Give the extent of all uninfected red blood cells.
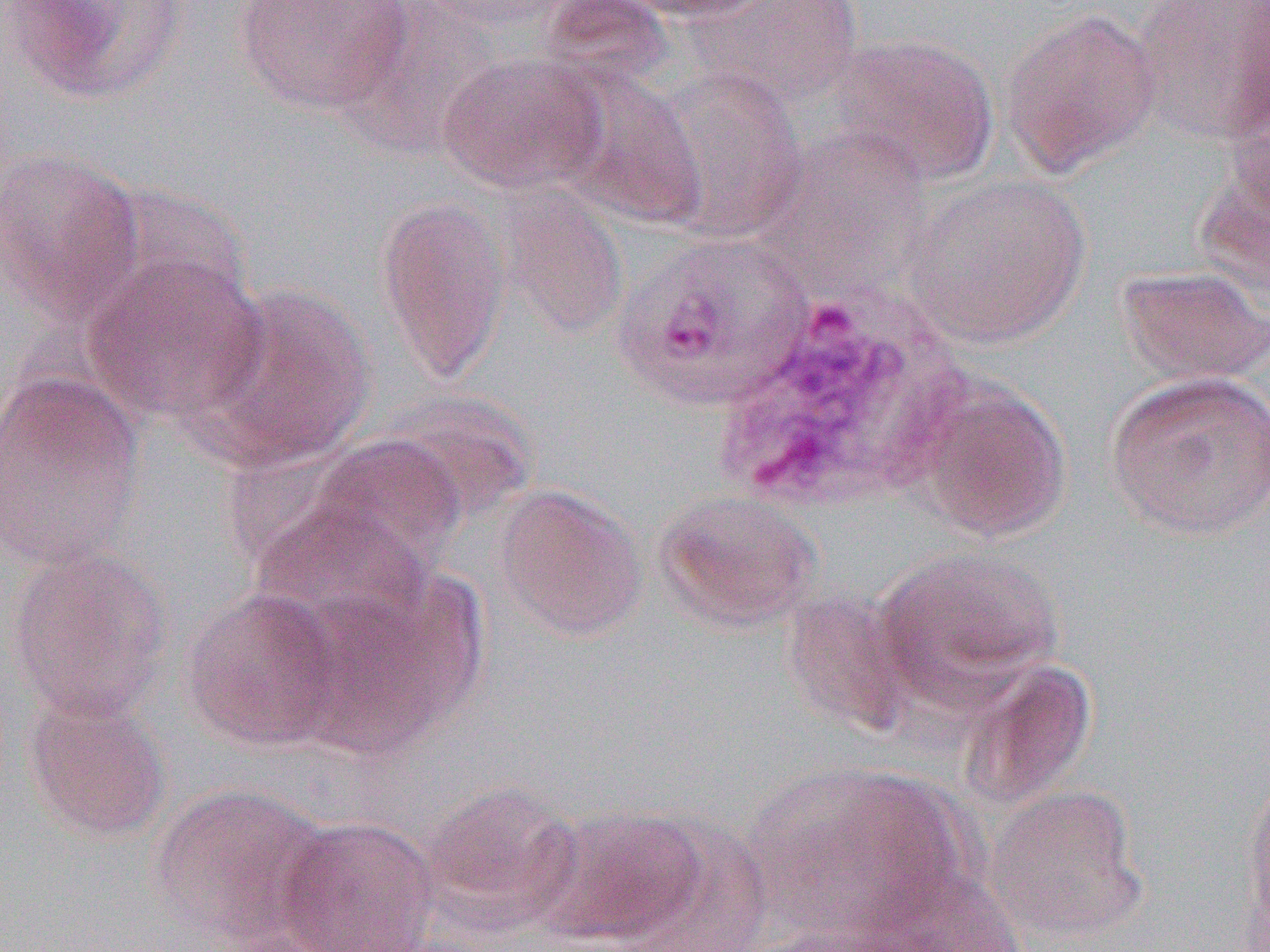
Approximate bounding boxes as (x1, y1, x2, y2) in pixels.
Uninfected red blood cells: (7, 0, 193, 104), (233, 0, 414, 116), (336, 0, 501, 159), (412, 0, 583, 32), (608, 0, 779, 23), (689, 1, 865, 110), (1133, 1, 1270, 145), (1000, 7, 1163, 176), (822, 34, 1001, 189), (437, 52, 608, 195), (546, 60, 707, 228), (655, 66, 808, 241), (762, 129, 933, 286), (0, 146, 145, 327), (1193, 148, 1270, 313), (903, 173, 1092, 350), (495, 183, 629, 340), (375, 193, 510, 386), (612, 230, 816, 411), (80, 250, 268, 427), (1115, 265, 1269, 387), (193, 284, 377, 470), (0, 370, 145, 570), (1104, 371, 1270, 540), (907, 377, 1073, 545), (377, 390, 539, 527), (305, 434, 468, 576), (494, 485, 649, 642), (652, 490, 823, 634), (249, 499, 438, 647), (3, 545, 174, 724), (873, 546, 1063, 709), (292, 572, 485, 755), (181, 587, 346, 753), (781, 588, 919, 739), (953, 658, 1097, 813), (21, 691, 173, 843), (1238, 761, 1270, 947), (747, 763, 970, 945), (148, 781, 335, 948), (420, 781, 584, 931), (986, 784, 1150, 945), (535, 806, 709, 947), (623, 814, 773, 951), (274, 815, 441, 952), (853, 865, 1024, 952).

Slide-level diagnosis: Plasmodium vivax. One field of a larger specimen. Thin blood film. Image is 1270×952 pixels. Optical microscopy. 1000x magnification.